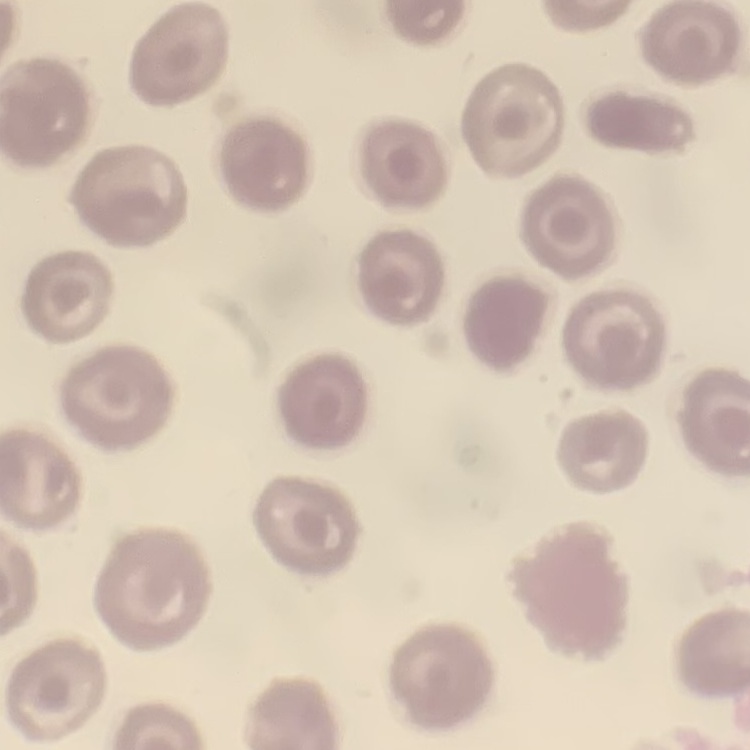

Summary:
  - Erythrocyte morphology: no rouleaux formation
  - Preparation: thin blood smear
  - Image type: square crop of a larger photomicrograph
  - Stain: Field's or Giemsa